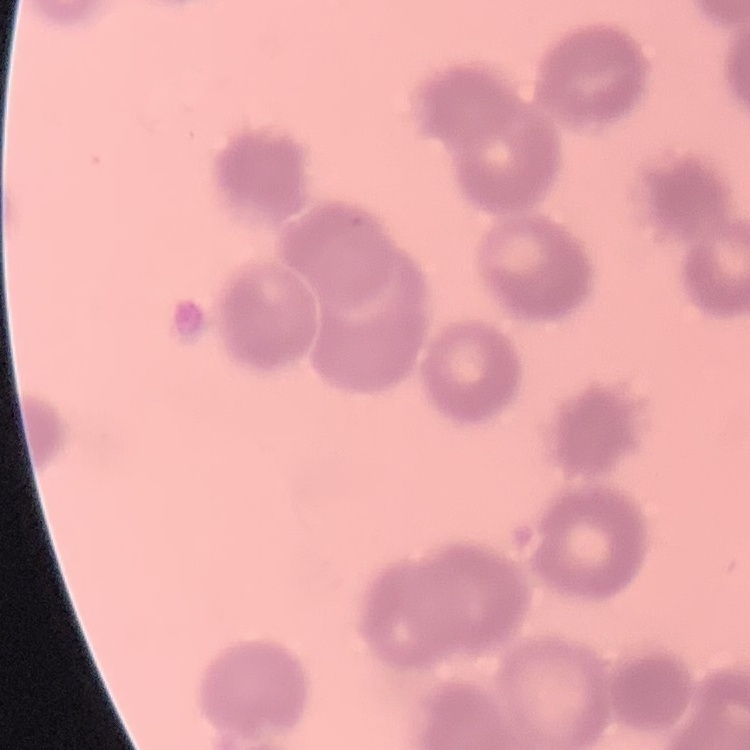

{
  "red_blood_cell_morphology": "rouleaux formation",
  "stain": "Field's or Giemsa",
  "image_type": "square crop of a larger photomicrograph",
  "preparation": "thin peripheral smear"
}